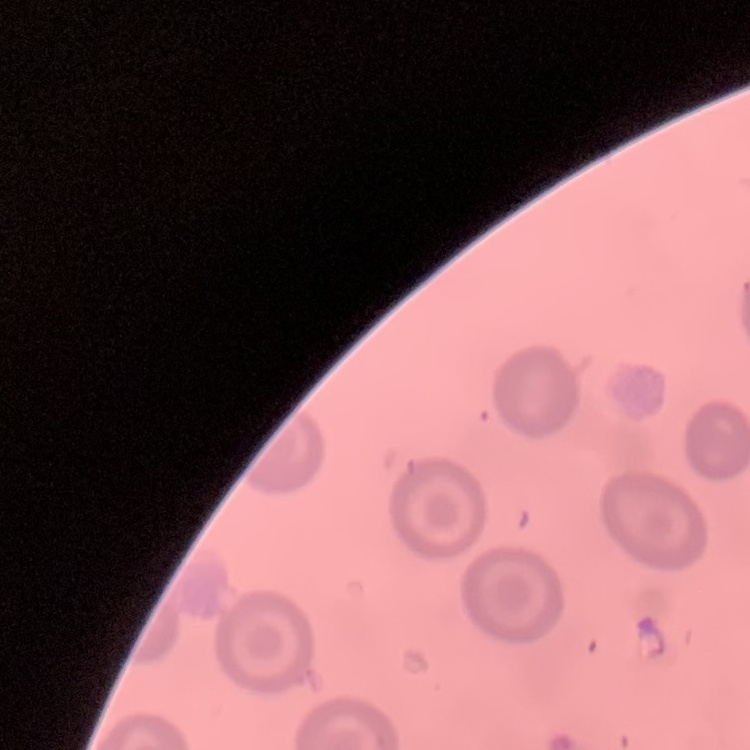

erythrocyte morphology = no rouleaux formation
image type = square crop of a larger photomicrograph
stain = Field's or Giemsa
preparation = thin blood smear